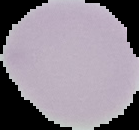

Summary:
  - Preparation: thin blood film
  - Result: negative for Plasmodium parasites
  - Image size: 139×130 pixels
  - Image type: segmented cell region on a black background